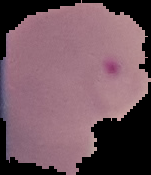
From a thin blood smear. Malaria status: parasitized. Cell region segmented out of the field of view; the surrounding area is masked to black. Image is 151×175 pixels.